Locate platelets.
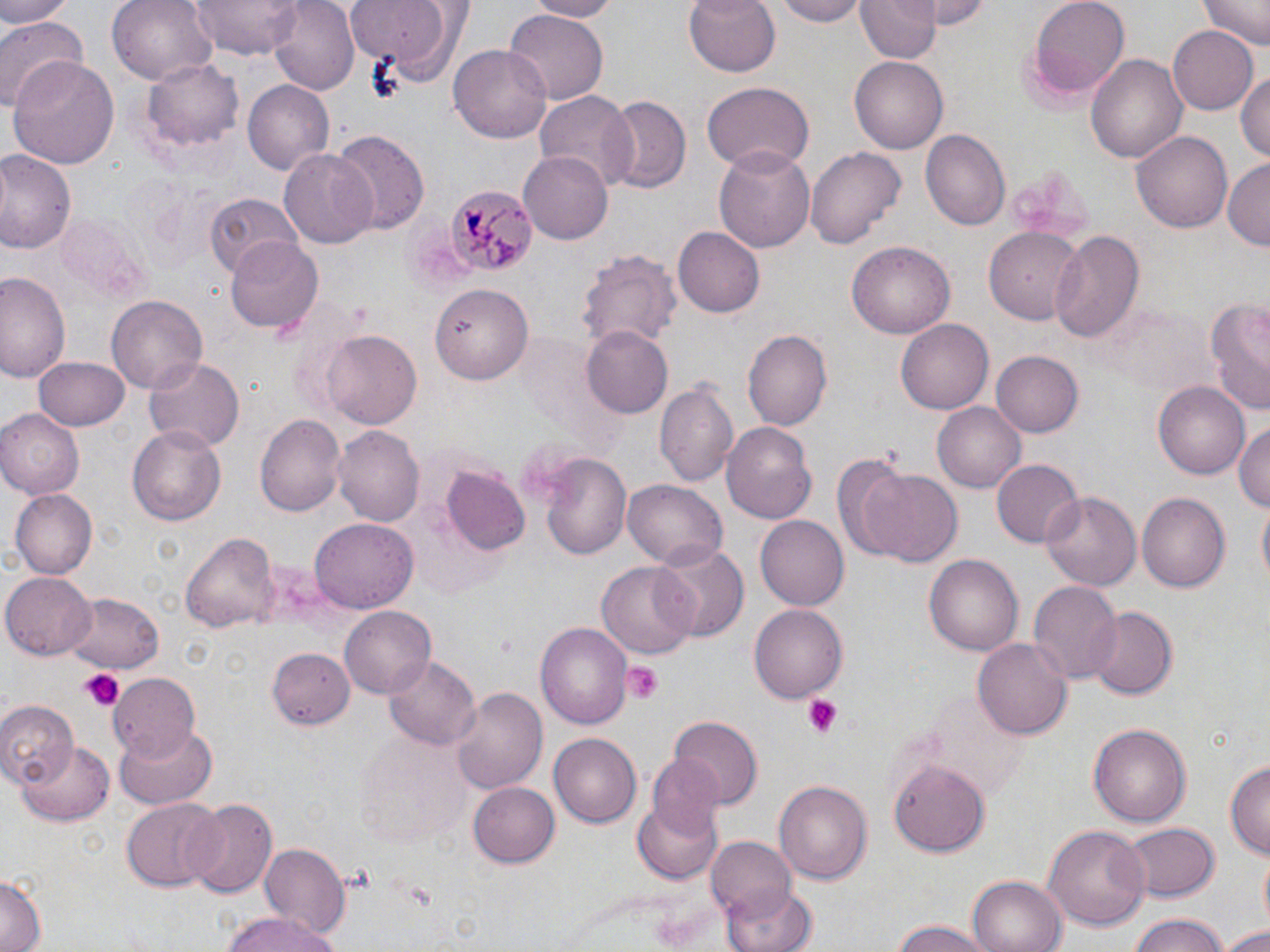

Approximate bounding boxes as named x1/y1/x2/y2 corners in pixels.
Platelets: (x1=623, y1=661, x2=665, y2=700), (x1=80, y1=670, x2=123, y2=710), (x1=803, y1=697, x2=843, y2=739).

plasmodium_malariae_infected_red_blood_cell_locations: 'approximate bounding boxes as named x1/y1/x2/y2 corners in pixels: (x1=445, y1=183, x2=531, y2=277)'
slide_level_diagnosis: Plasmodium malariae
uninfected_red_blood_cell_locations: 'approximate bounding boxes as named x1/y1/x2/y2 corners in pixels: (x1=0, y1=0, x2=75, y2=25), (x1=191, y1=0, x2=302, y2=57), (x1=268, y1=0, x2=361, y2=94), (x1=523, y1=0, x2=616, y2=20), (x1=684, y1=0, x2=782, y2=77), (x1=768, y1=0, x2=871, y2=25), (x1=854, y1=0, x2=939, y2=65), (x1=925, y1=0, x2=997, y2=28), (x1=1025, y1=0, x2=1132, y2=100), (x1=1202, y1=0, x2=1268, y2=49), (x1=108, y1=1, x2=218, y2=88), (x1=344, y1=1, x2=469, y2=85), (x1=505, y1=11, x2=609, y2=102), (x1=0, y1=13, x2=89, y2=112), (x1=1168, y1=26, x2=1259, y2=115), (x1=450, y1=42, x2=552, y2=145), (x1=1086, y1=51, x2=1187, y2=168), (x1=10, y1=54, x2=119, y2=170), (x1=138, y1=56, x2=245, y2=159), (x1=849, y1=56, x2=947, y2=154), (x1=1235, y1=68, x2=1269, y2=164), (x1=240, y1=78, x2=335, y2=175), (x1=703, y1=80, x2=812, y2=172), (x1=533, y1=92, x2=636, y2=188), (x1=603, y1=96, x2=689, y2=194), (x1=919, y1=130, x2=1009, y2=231), (x1=1132, y1=130, x2=1231, y2=236), (x1=329, y1=131, x2=430, y2=235), (x1=805, y1=144, x2=907, y2=251), (x1=714, y1=145, x2=816, y2=255), (x1=279, y1=149, x2=377, y2=250), (x1=0, y1=151, x2=77, y2=254), (x1=519, y1=152, x2=612, y2=242), (x1=1222, y1=158, x2=1270, y2=250), (x1=204, y1=192, x2=299, y2=276), (x1=58, y1=212, x2=150, y2=302), (x1=1049, y1=227, x2=1145, y2=343), (x1=674, y1=228, x2=764, y2=317), (x1=984, y1=229, x2=1083, y2=324), (x1=226, y1=238, x2=325, y2=335), (x1=847, y1=242, x2=954, y2=339), (x1=577, y1=246, x2=681, y2=350), (x1=0, y1=271, x2=67, y2=382), (x1=0, y1=277, x2=125, y2=398), (x1=431, y1=282, x2=534, y2=383), (x1=104, y1=295, x2=208, y2=397), (x1=1203, y1=296, x2=1270, y2=415), (x1=1100, y1=302, x2=1212, y2=395), (x1=897, y1=317, x2=992, y2=412), (x1=580, y1=327, x2=672, y2=418), (x1=321, y1=329, x2=423, y2=431), (x1=742, y1=329, x2=831, y2=431), (x1=991, y1=351, x2=1083, y2=438), (x1=32, y1=356, x2=130, y2=430), (x1=145, y1=357, x2=244, y2=454), (x1=655, y1=378, x2=738, y2=489), (x1=1153, y1=382, x2=1250, y2=480), (x1=932, y1=402, x2=1026, y2=493), (x1=0, y1=409, x2=83, y2=498), (x1=256, y1=413, x2=347, y2=519), (x1=1234, y1=419, x2=1269, y2=514), (x1=721, y1=421, x2=817, y2=525), (x1=128, y1=426, x2=227, y2=525), (x1=333, y1=426, x2=423, y2=526), (x1=538, y1=450, x2=632, y2=562), (x1=831, y1=450, x2=929, y2=564), (x1=992, y1=460, x2=1082, y2=549), (x1=440, y1=466, x2=532, y2=558), (x1=861, y1=467, x2=964, y2=568), (x1=622, y1=477, x2=727, y2=567), (x1=10, y1=489, x2=96, y2=579), (x1=1042, y1=490, x2=1141, y2=592), (x1=1138, y1=493, x2=1231, y2=593), (x1=755, y1=516, x2=847, y2=610), (x1=311, y1=517, x2=418, y2=614), (x1=182, y1=531, x2=280, y2=635), (x1=654, y1=541, x2=749, y2=640), (x1=925, y1=554, x2=1024, y2=655), (x1=598, y1=559, x2=699, y2=661), (x1=2, y1=573, x2=96, y2=659), (x1=1028, y1=582, x2=1121, y2=684), (x1=66, y1=592, x2=164, y2=672), (x1=749, y1=603, x2=847, y2=702), (x1=340, y1=606, x2=437, y2=697), (x1=1084, y1=606, x2=1181, y2=699), (x1=536, y1=620, x2=632, y2=732), (x1=975, y1=637, x2=1072, y2=741), (x1=265, y1=647, x2=355, y2=734), (x1=384, y1=655, x2=481, y2=752), (x1=107, y1=672, x2=201, y2=755), (x1=452, y1=686, x2=548, y2=796), (x1=0, y1=699, x2=76, y2=785), (x1=670, y1=716, x2=761, y2=807), (x1=113, y1=722, x2=219, y2=809), (x1=1087, y1=722, x2=1191, y2=830), (x1=355, y1=729, x2=468, y2=848), (x1=549, y1=732, x2=641, y2=826), (x1=16, y1=742, x2=115, y2=825), (x1=645, y1=754, x2=730, y2=844), (x1=1226, y1=756, x2=1269, y2=860), (x1=887, y1=758, x2=995, y2=856), (x1=774, y1=779, x2=872, y2=884), (x1=468, y1=780, x2=560, y2=866), (x1=183, y1=798, x2=278, y2=901), (x1=121, y1=799, x2=221, y2=891), (x1=633, y1=799, x2=722, y2=884), (x1=1122, y1=822, x2=1220, y2=901), (x1=1044, y1=824, x2=1151, y2=932), (x1=707, y1=838, x2=799, y2=922), (x1=260, y1=842, x2=348, y2=936), (x1=0, y1=876, x2=44, y2=952), (x1=966, y1=876, x2=1065, y2=952), (x1=724, y1=881, x2=816, y2=952), (x1=218, y1=913, x2=342, y2=952), (x1=1125, y1=915, x2=1239, y2=952), (x1=888, y1=920, x2=995, y2=952), (x1=1221, y1=925, x2=1270, y2=952)'
field_of_view: one of a larger specimen
stain: May-Grünwald-Giemsa
modality: light microscopy
preparation: thin blood film
magnification: 1000x
image_size: 1270×952 pixels